Locate every uninfected red blood cell.
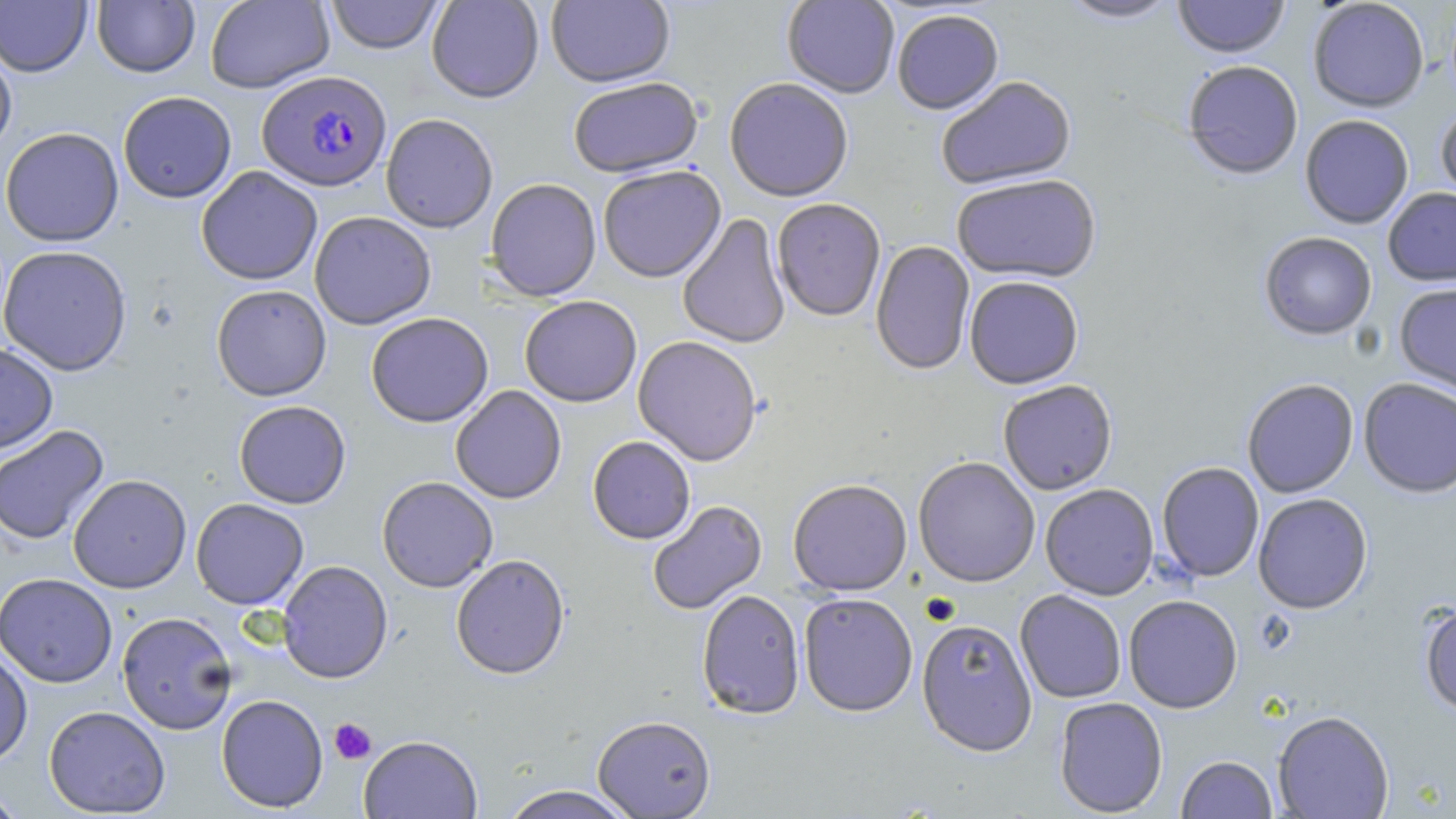
Approximate bounding boxes as (x1, y1, x2, y2) in pixels.
Uninfected red blood cells: (205, 0, 335, 93), (325, 0, 444, 55), (427, 0, 544, 104), (546, 0, 675, 89), (782, 0, 900, 99), (1059, 0, 1180, 25), (1172, 0, 1290, 60), (1308, 0, 1430, 113), (0, 1, 92, 76), (92, 1, 200, 77), (892, 10, 1004, 117), (0, 40, 17, 159), (1182, 62, 1303, 182), (937, 77, 1077, 192), (567, 79, 703, 180), (724, 80, 854, 204), (118, 91, 237, 203), (1435, 105, 1456, 207), (381, 113, 498, 233), (1300, 115, 1414, 229), (1, 127, 124, 247), (196, 166, 323, 285), (598, 166, 725, 283), (951, 176, 1101, 285), (485, 178, 601, 303), (1382, 187, 1456, 286), (772, 200, 886, 323), (309, 211, 436, 329), (677, 213, 791, 350), (1259, 232, 1377, 341), (870, 241, 975, 376), (0, 244, 132, 376), (964, 276, 1084, 389), (1394, 282, 1456, 398), (210, 284, 332, 401), (519, 296, 642, 407), (366, 312, 493, 428), (633, 336, 763, 467), (0, 342, 59, 453), (1358, 378, 1456, 498), (1242, 379, 1359, 498), (998, 380, 1118, 495), (450, 386, 566, 504), (234, 400, 351, 508), (0, 424, 109, 546), (587, 436, 695, 544), (913, 457, 1040, 587), (1156, 462, 1265, 582), (68, 474, 191, 593), (377, 476, 498, 592), (1155, 479, 1375, 592), (788, 480, 912, 596), (1040, 484, 1159, 600), (1253, 493, 1373, 614), (191, 498, 309, 610), (647, 500, 768, 615), (451, 554, 570, 679), (278, 560, 393, 683), (0, 573, 118, 687), (696, 589, 805, 719), (1015, 590, 1127, 703), (798, 593, 917, 717), (1123, 595, 1243, 713), (1419, 601, 1456, 716), (116, 611, 237, 734), (916, 618, 1037, 756), (0, 646, 33, 766), (216, 694, 328, 813), (1054, 697, 1168, 817), (43, 705, 170, 817), (1273, 711, 1394, 818), (592, 715, 715, 818), (359, 735, 482, 818), (1176, 755, 1277, 818), (497, 785, 639, 819), (0, 786, 28, 818).

slide_level_diagnosis: Plasmodium falciparum
image_size: 1456×819 pixels
magnification: 1000x
platelet_locations: 'approximate bounding boxes as (x1, y1, x2, y2) in pixels: (328, 718, 376, 764)'
plasmodium_falciparum_infected_red_blood_cell_locations: 'approximate bounding boxes as (x1, y1, x2, y2) in pixels: (257, 70, 392, 191)'
field_of_view: single
preparation: thin blood film
stain: May-Grünwald-Giemsa
modality: light microscopy